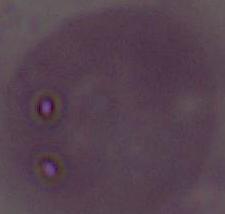

magnification = 1000x
identification = red blood cell
modality = photomicrograph